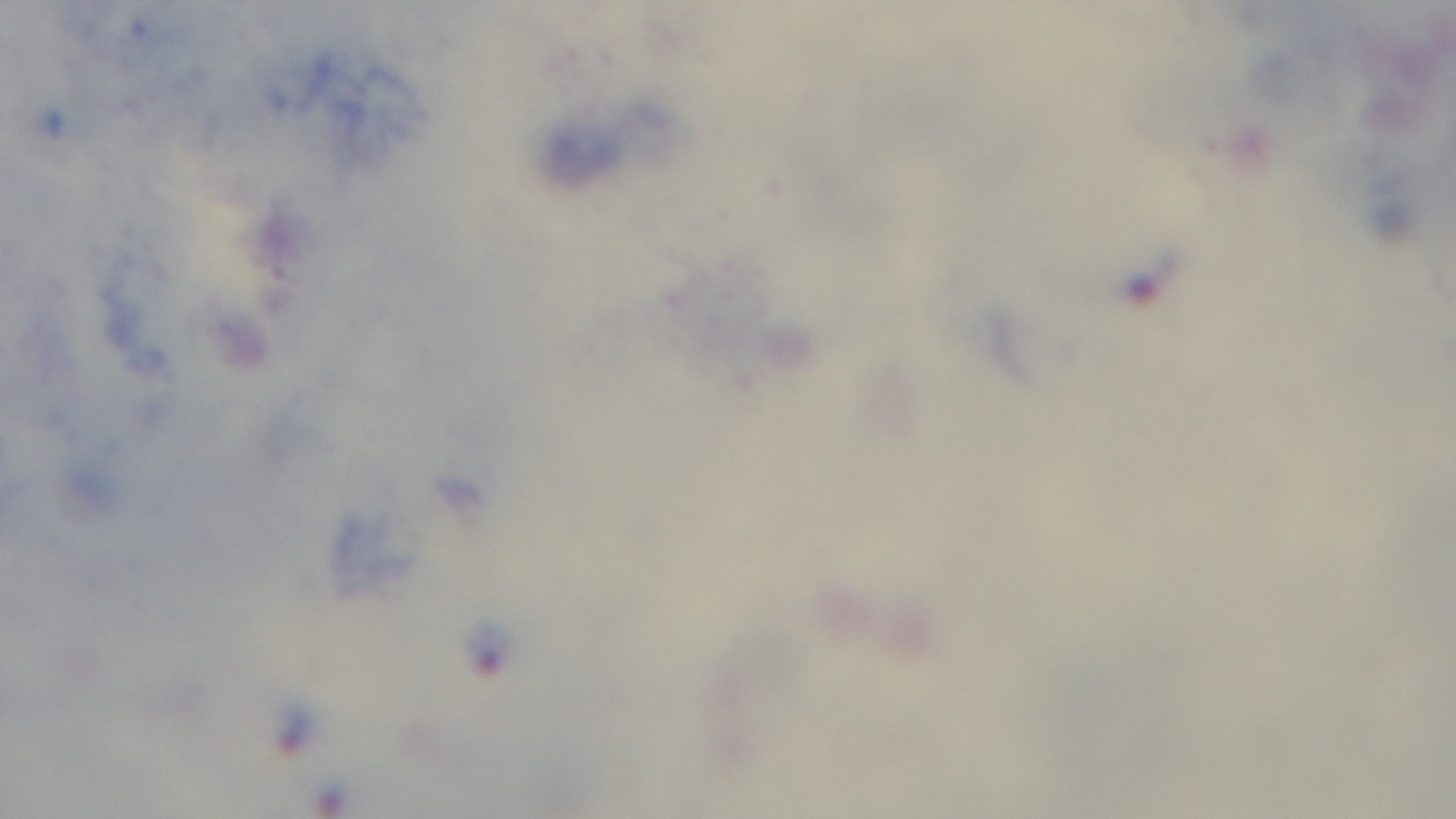
{
  "malaria_status": "infected",
  "modality": "light microscopy",
  "field_of_view": "single",
  "stain": "Giemsa",
  "capture": "mounted 4K digital camera",
  "objective": "100x oil immersion",
  "preparation": "thick"
}